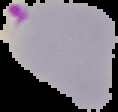

preparation = thin blood film
image type = segmented cell region with the area outside set to black
image size = 118×112 pixels
result = Plasmodium parasites identified